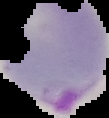
malaria status = parasitized
image size = 109×118 pixels
image type = cell region segmented out of the field of view; surrounding area masked to black
preparation = thin blood film